Name the parasite shown.
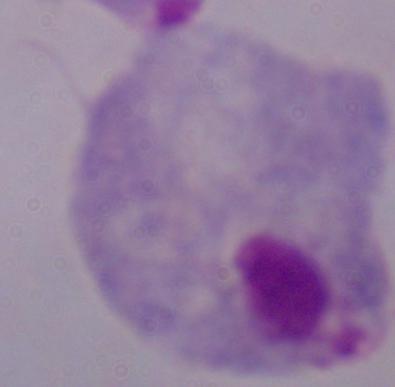

A trichomonad.

{
  "magnification": "1000x",
  "modality": "photomicrograph"
}